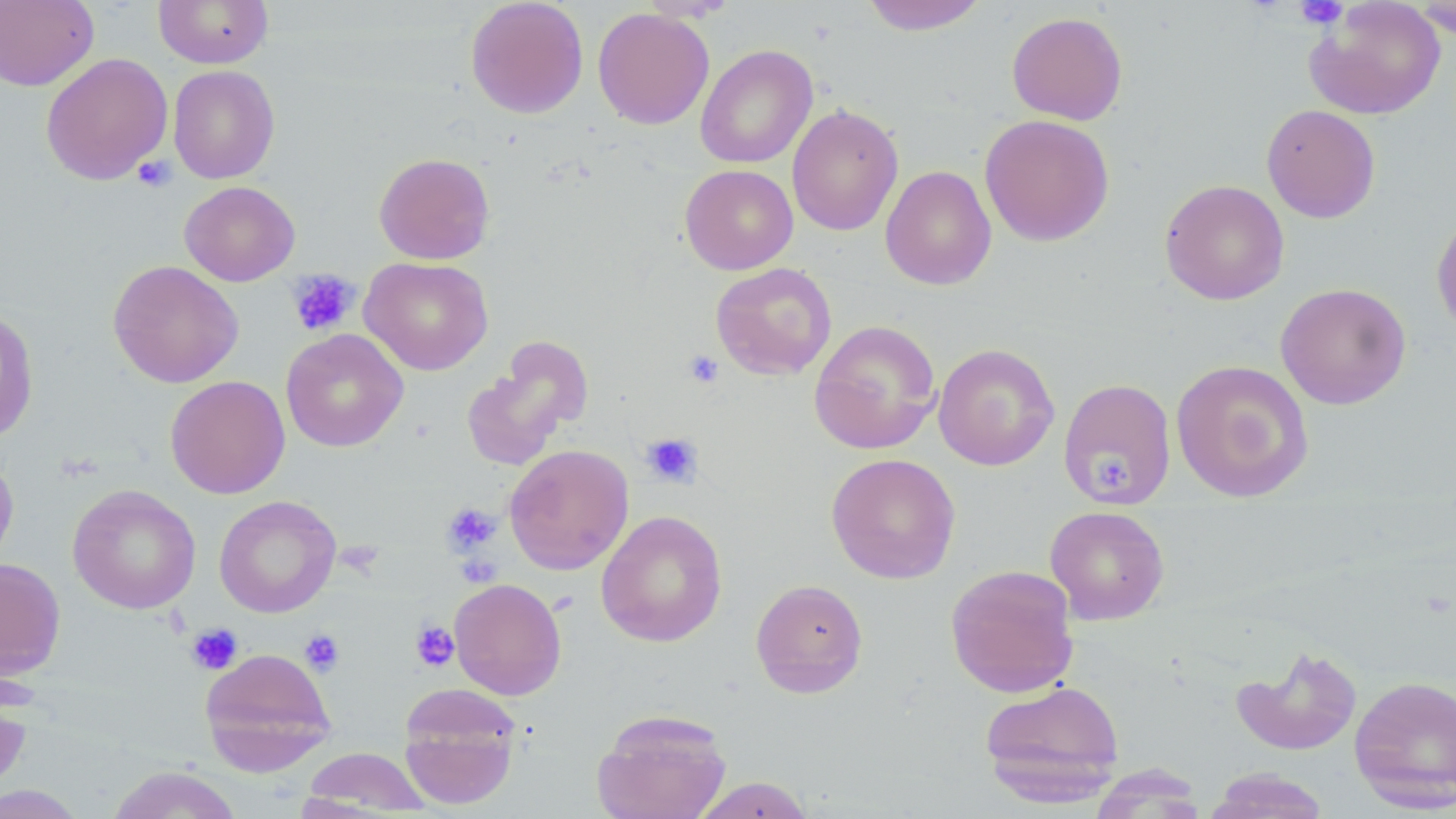
Approximate bounding boxes as (x1,y1)-(x2,y2) corner pairs in pixels. Platelet locations: (1294,1)-(1349,29), (132,155)-(176,192), (287,270)-(360,336), (683,349)-(724,389), (640,433)-(703,488), (1091,450)-(1136,498), (442,502)-(502,556), (410,620)-(459,671), (186,623)-(242,675), (299,630)-(345,676). Uninfected red blood cell locations: (0,0)-(98,91), (154,0)-(273,68), (465,0)-(589,118), (637,0)-(740,22), (860,0)-(989,35), (1409,0)-(1456,39), (1305,1)-(1446,120), (592,7)-(714,130), (1006,11)-(1128,125), (695,45)-(817,169), (40,52)-(173,185), (168,65)-(280,184), (787,104)-(903,236), (1261,104)-(1381,223), (979,114)-(1115,246), (374,152)-(494,264), (680,164)-(798,274), (880,165)-(996,290), (1159,179)-(1290,305), (180,180)-(300,286), (1431,210)-(1456,337), (359,256)-(493,375), (108,260)-(244,388), (711,263)-(837,380), (1275,282)-(1412,410), (0,307)-(40,445), (809,320)-(942,455), (281,328)-(409,452), (460,342)-(588,472), (933,343)-(1060,471), (1171,359)-(1314,502), (165,376)-(290,499), (1059,378)-(1177,508), (504,444)-(634,575), (0,451)-(19,573), (826,453)-(961,584), (67,483)-(201,614), (214,495)-(341,618), (1044,505)-(1170,625), (596,510)-(728,647), (0,558)-(66,680), (945,564)-(1080,698), (449,578)-(566,699), (750,579)-(869,698), (1231,644)-(1363,756), (198,646)-(337,775), (1349,675)-(1456,810), (0,676)-(33,800), (979,679)-(1125,804), (398,686)-(523,809), (592,709)-(732,819), (299,747)-(433,815), (106,765)-(243,819), (1205,768)-(1331,818), (689,776)-(816,818), (0,783)-(88,818). Slide-level diagnosis: negative for blood parasites. Image is 1456×819 pixels. May-Grünwald-Giemsa stain. Captured at 1000x magnification. Single field of view. Thin blood film. Optical microscopy.